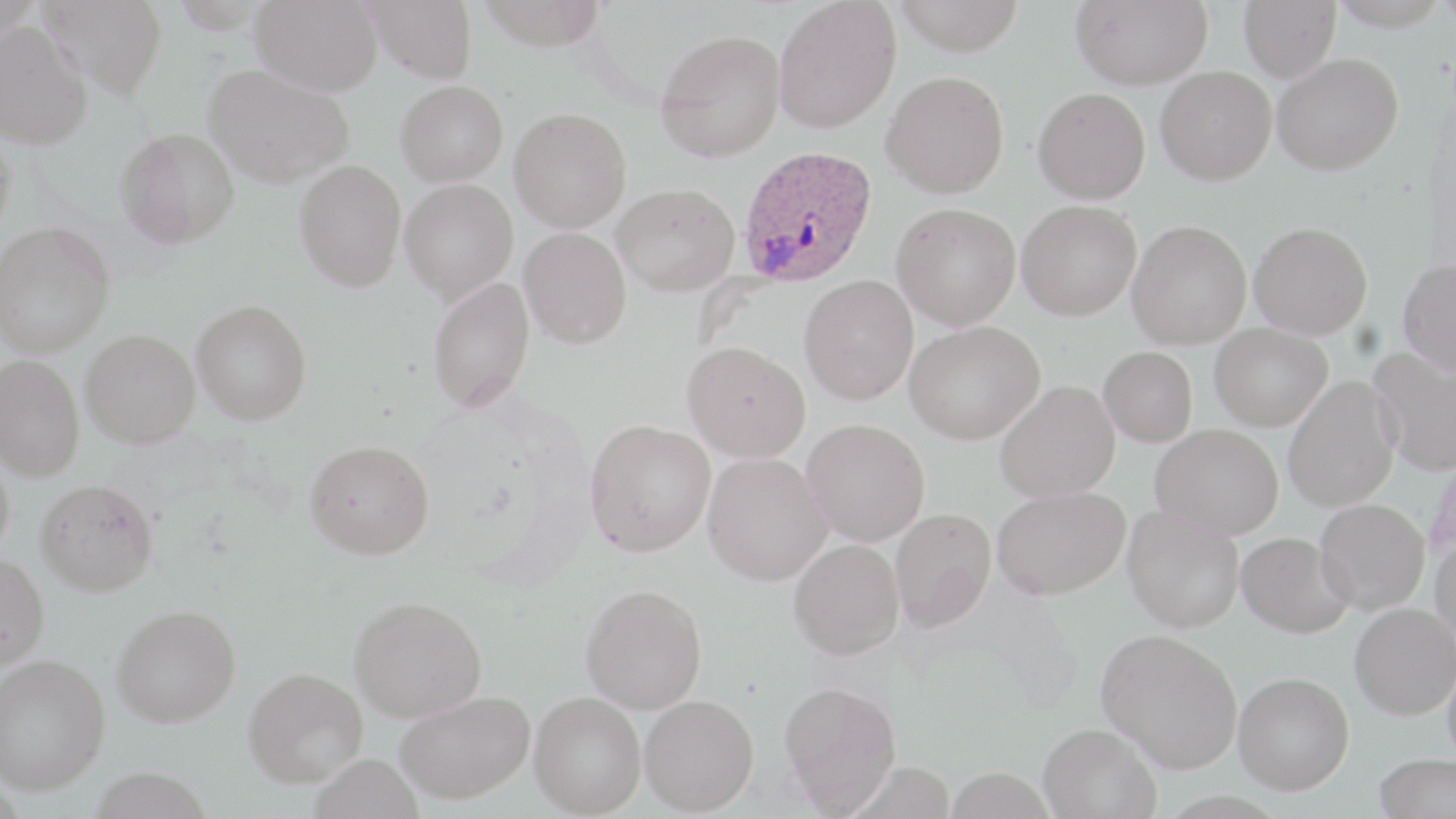

Approximate bounding boxes as [x1, y1, x2, y2] in pixels. Uninfected red blood cell locations: [39, 0, 168, 99], [251, 0, 383, 95], [362, 0, 477, 83], [475, 0, 609, 50], [892, 0, 1024, 56], [1071, 0, 1213, 89], [1239, 0, 1341, 82], [1326, 0, 1452, 31], [773, 1, 902, 134], [0, 22, 93, 150], [656, 29, 786, 162], [1272, 52, 1404, 175], [203, 63, 354, 187], [1156, 66, 1276, 185], [882, 70, 1010, 198], [395, 80, 508, 187], [1033, 87, 1151, 204], [509, 107, 632, 232], [0, 125, 16, 246], [115, 127, 239, 249], [294, 159, 406, 292], [400, 178, 518, 302], [611, 183, 739, 296], [1016, 200, 1141, 320], [892, 202, 1021, 330], [1127, 219, 1252, 349], [0, 221, 115, 358], [1249, 221, 1373, 339], [519, 226, 632, 348], [1397, 258, 1456, 378], [799, 274, 919, 405], [427, 276, 535, 412], [191, 298, 312, 425], [904, 320, 1045, 444], [1209, 323, 1332, 431], [80, 329, 200, 448], [682, 341, 810, 462], [1098, 346, 1198, 447], [1367, 347, 1456, 476], [0, 354, 84, 482], [1283, 376, 1400, 512], [994, 380, 1120, 502], [801, 418, 930, 547], [585, 419, 715, 556], [1150, 424, 1284, 538], [305, 439, 435, 560], [0, 449, 15, 565], [702, 452, 832, 586], [1426, 452, 1456, 566], [35, 478, 158, 596], [991, 486, 1130, 600], [1315, 498, 1430, 614], [1122, 505, 1244, 633], [889, 507, 997, 631], [1237, 531, 1355, 638], [1429, 531, 1456, 649], [788, 538, 904, 659], [0, 553, 49, 672], [580, 583, 707, 714], [349, 596, 486, 722], [1349, 602, 1455, 720], [111, 604, 241, 728], [1096, 628, 1242, 773], [1443, 649, 1456, 772], [0, 653, 110, 795], [243, 666, 368, 787], [1234, 672, 1354, 794], [779, 680, 902, 813], [394, 690, 534, 805], [529, 691, 646, 817], [639, 693, 759, 815], [1038, 722, 1161, 818], [1374, 753, 1455, 818]. Plasmodium ovale-infected red blood cell locations: [738, 145, 876, 287]. Slide-level diagnosis: Plasmodium ovale. One field of a larger specimen. Image is 1456×819 pixels. Thin blood smear. Captured at 1000x magnification. Optical microscopy. May-Grünwald-Giemsa stain.